Identify the cell.
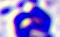

A leukocyte.

Micrograph. Captured at 400x magnification.